Name the parasite shown.
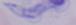
A trypanosome.

1000x magnification. Photomicrograph.